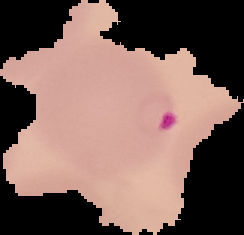

malaria status = parasitized
image type = segmented cell region with the area outside set to black
preparation = thin blood film
image size = 244×235 pixels